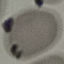 Malaria status: uninfected. Cell patch, automatically extracted from a larger field of view and resized to 64 × 64 pixels. Giemsa-stained preparation. Acquired by smartphone through the microscope eyepiece. Thin smear of blood.